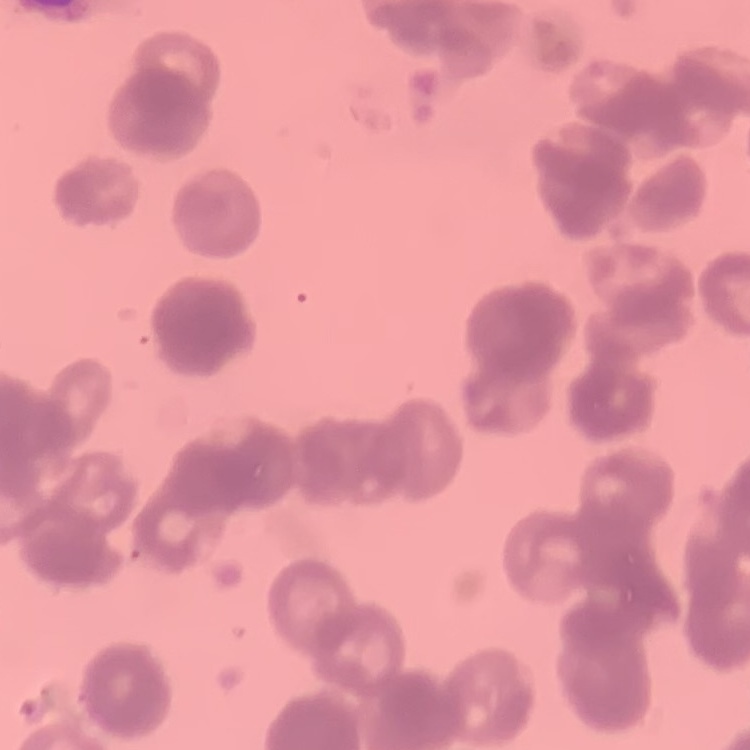
The erythrocytes show rouleaux formation. Stained with either Field's or Giemsa. Square crop of a larger photomicrograph. Thin blood film.